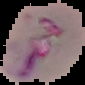

Result: malaria parasites identified. Cell region segmented out of the field of view; the surrounding area is masked to black. Image is 85×85 pixels. From a thin blood smear.